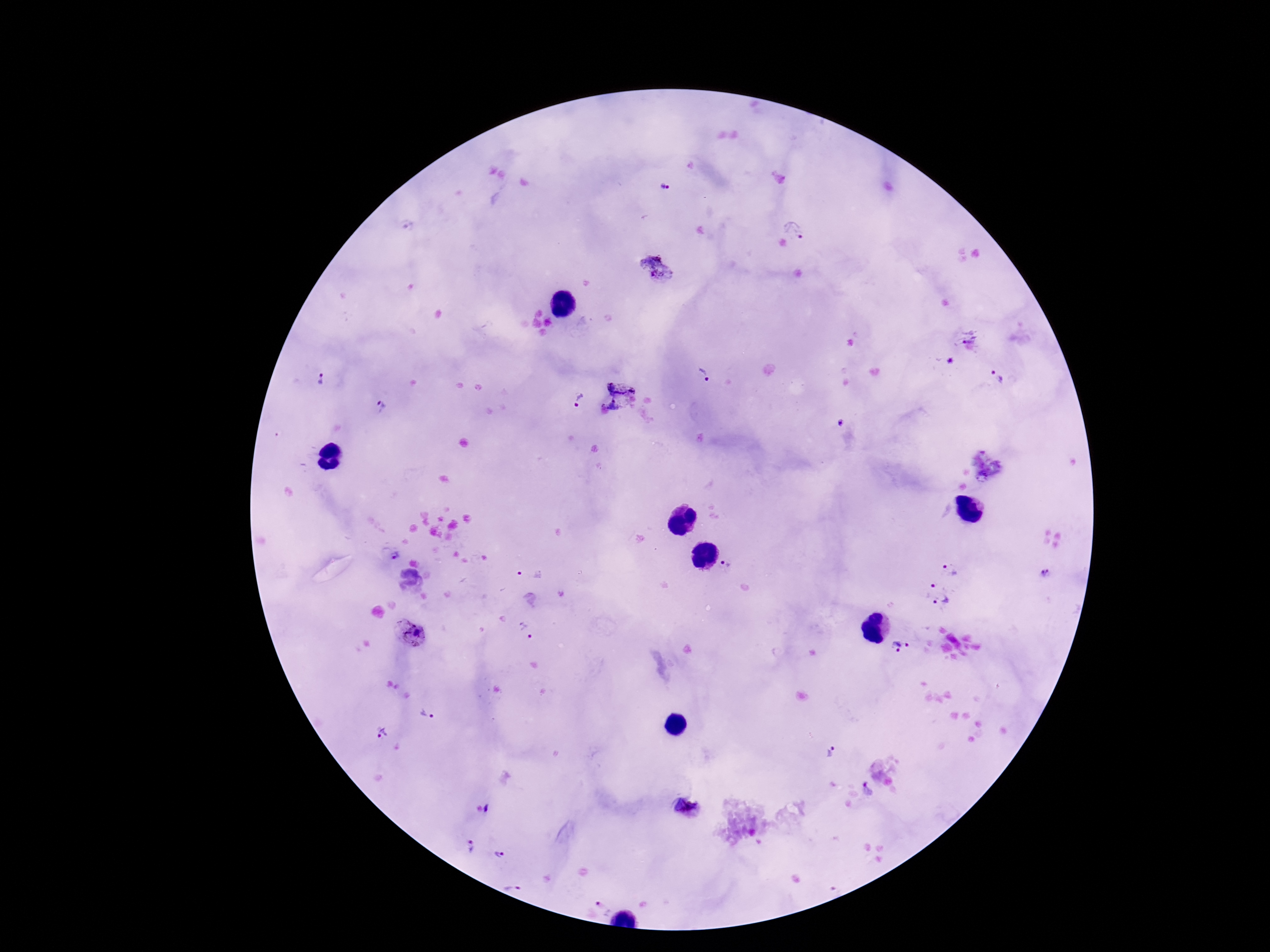

Approximate centers as (x, y) in pixels.
Summary:
  - Plasmodium parasite locations: (665, 187), (793, 229), (657, 270), (969, 336), (623, 377), (996, 377), (704, 378), (321, 379), (577, 400), (381, 406), (614, 409), (839, 423), (396, 554), (727, 566), (949, 569), (530, 572), (1047, 574), (934, 585), (943, 603), (526, 631), (411, 633), (901, 647), (427, 714), (382, 733), (831, 752), (868, 789), (489, 808), (472, 847), (498, 855), (512, 887), (601, 903)
  - Patient malaria status: positive
  - Capture: smartphone camera through the microscope eyepiece
  - Stain: Giemsa
  - Image size: 1270×952 pixels
  - Field of view: single
  - Preparation: thick blood smear
  - Magnification: 100x